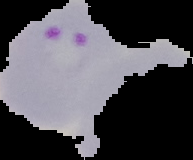 Cell region segmented out of the field of view; the surrounding area is masked to black. Result: malaria parasites identified. Image is 193×160 pixels. From a thin blood film.